State the blood parasite species.
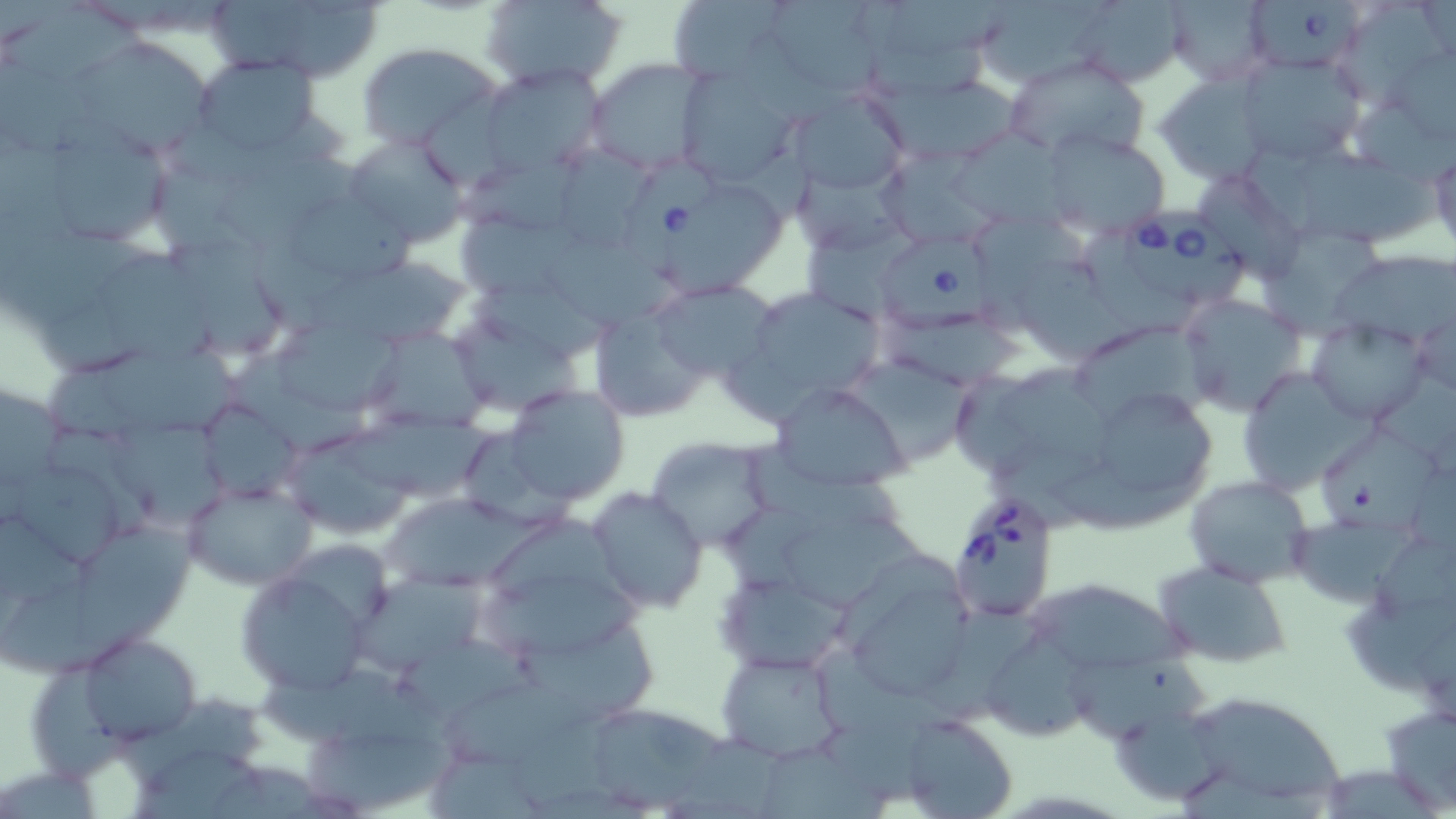

Babesia divergens.

Approximate bounding boxes as (x1, y1, x2, y2) in pixels. Babesia divergens-infected red blood cell locations: (1243, 3, 1366, 82), (624, 162, 733, 289), (1117, 202, 1256, 307), (872, 234, 1012, 335), (947, 489, 1062, 625). Uninfected red blood cell locations: (208, 0, 389, 83), (480, 0, 627, 91), (669, 0, 796, 86), (1164, 0, 1274, 85), (1081, 1, 1204, 92), (980, 2, 1111, 85), (1, 9, 153, 85), (67, 36, 214, 157), (355, 41, 500, 149), (1236, 54, 1363, 165), (193, 56, 322, 157), (1006, 56, 1152, 158), (585, 58, 706, 174), (479, 64, 605, 176), (863, 65, 1035, 165), (683, 71, 802, 187), (1159, 74, 1271, 186), (790, 91, 910, 196), (32, 123, 180, 252), (1044, 128, 1170, 233), (948, 132, 1084, 238), (341, 134, 470, 248), (548, 141, 663, 249), (213, 148, 393, 255), (1295, 148, 1442, 254), (1428, 150, 1455, 252), (672, 187, 789, 296), (451, 204, 585, 304), (1265, 223, 1390, 346), (544, 237, 685, 325), (175, 238, 289, 363), (1330, 251, 1456, 342), (94, 254, 220, 376), (303, 272, 477, 345), (731, 285, 889, 416), (651, 290, 792, 387), (1177, 292, 1311, 417), (596, 313, 722, 425), (271, 315, 409, 424), (1306, 319, 1430, 424), (458, 320, 591, 425), (1073, 320, 1226, 425), (369, 324, 497, 436), (99, 345, 252, 442), (849, 357, 986, 470), (991, 363, 1132, 470), (1243, 369, 1374, 506), (771, 382, 910, 490), (504, 385, 629, 506), (1098, 398, 1223, 497), (341, 415, 513, 506), (1320, 422, 1441, 542), (286, 432, 430, 547), (645, 436, 779, 554), (8, 450, 140, 571), (1183, 474, 1317, 589), (181, 476, 316, 592), (586, 489, 707, 611), (384, 492, 535, 592), (782, 512, 937, 611), (75, 527, 205, 659), (841, 555, 979, 703), (232, 562, 380, 698), (1153, 562, 1294, 668), (716, 567, 852, 674), (352, 571, 499, 680), (1024, 576, 1183, 674), (485, 577, 654, 669), (0, 582, 167, 680), (511, 610, 664, 728), (991, 627, 1102, 745), (74, 634, 201, 748), (1057, 649, 1230, 755), (719, 651, 846, 764), (257, 658, 444, 752), (446, 676, 608, 775), (1173, 689, 1350, 811), (1379, 699, 1456, 812), (590, 707, 733, 806), (1113, 711, 1248, 806), (898, 714, 1017, 819), (300, 723, 476, 813), (754, 745, 895, 819). Thin blood film. 1000x magnification. Image is 1456×819 pixels. One field of a larger specimen. Optical microscopy. May-Grünwald-Giemsa stain.